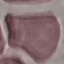
Result: no malaria parasites seen. Thin smear of blood. Giemsa-stained preparation. Photographed with a smartphone camera at the microscope eyepiece. Cell patch, automatically extracted from a larger field of view and resized to 64 × 64 pixels.